Identify the cell.
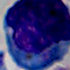
This is a leukocyte.

Captured at 1000x magnification. Micrograph.